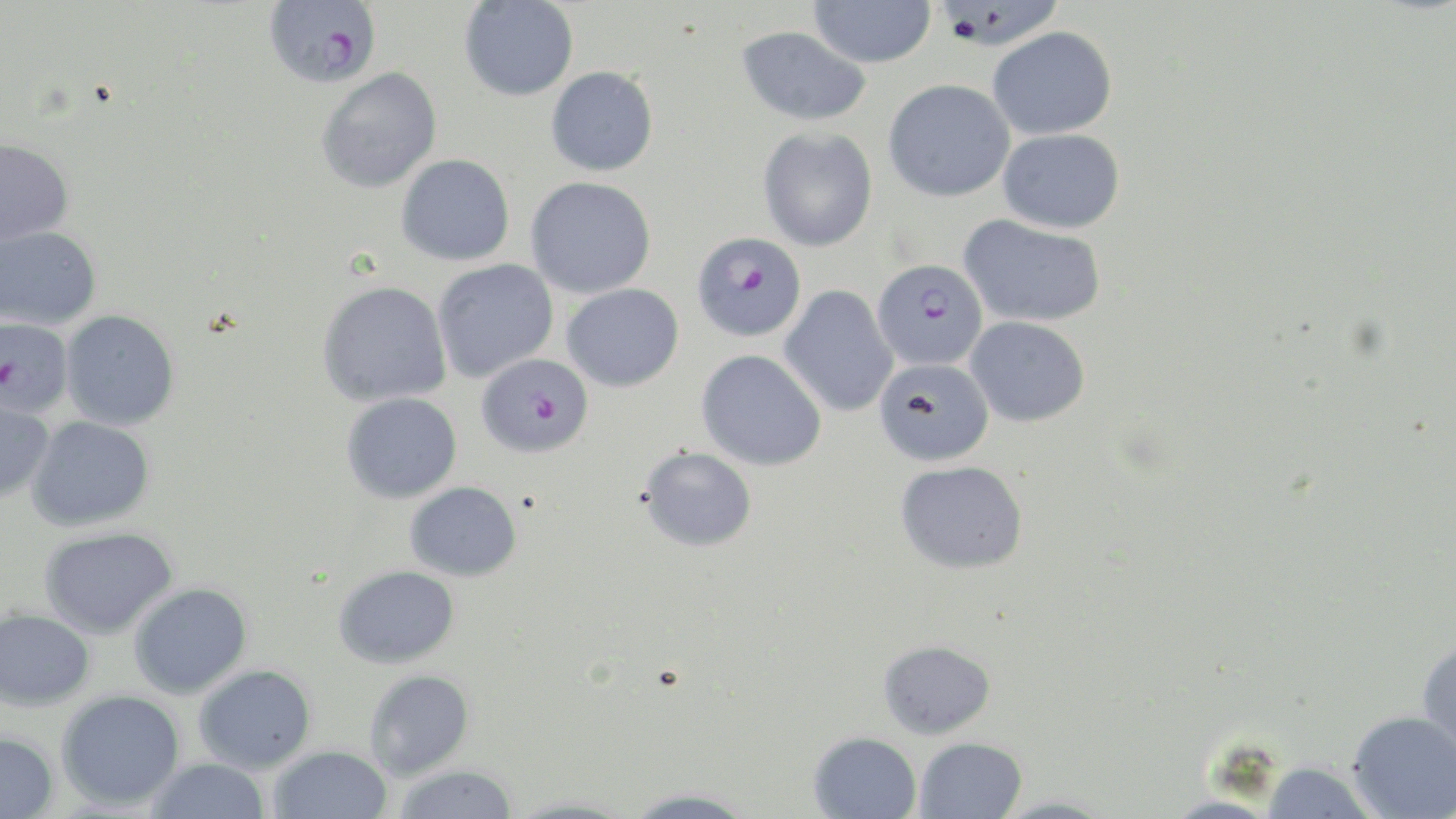 Approximate bounding boxes as (x1,y1)-(x2,y2) corner pairs in pixels. Uninfected red blood cell locations: (807,0)-(936,68), (459,1)-(578,101), (736,25)-(872,126), (986,26)-(1118,140), (546,66)-(658,176), (316,68)-(442,193), (883,79)-(1016,203), (757,127)-(878,251), (998,128)-(1127,233), (0,136)-(75,245), (397,154)-(515,265), (525,176)-(656,298), (959,213)-(1107,328), (0,225)-(102,329), (432,259)-(559,381), (317,280)-(452,407), (562,284)-(684,392), (779,285)-(898,417), (61,310)-(180,430), (966,316)-(1091,426), (696,350)-(826,471), (874,358)-(994,466), (341,392)-(462,504), (0,394)-(55,501), (26,416)-(155,531), (638,446)-(757,552), (894,460)-(1029,574), (405,481)-(522,581), (39,526)-(178,639), (333,565)-(460,668), (128,582)-(252,699), (0,608)-(96,710), (1416,637)-(1456,768), (878,639)-(995,738), (193,664)-(317,773), (363,669)-(475,780), (56,689)-(185,810), (1347,710)-(1456,819), (0,731)-(59,819), (807,731)-(922,819), (913,737)-(1027,819), (268,745)-(392,819), (145,756)-(271,818), (1260,761)-(1379,819), (391,763)-(520,819), (621,787)-(758,818), (992,794)-(1118,818). Plasmodium falciparum-infected red blood cell locations: (263,0)-(382,89), (692,232)-(806,342), (872,258)-(988,370), (0,315)-(74,419), (475,353)-(593,458). Slide-level diagnosis: Plasmodium falciparum. Light microscopy. May-Grünwald-Giemsa stain. Image is 1456×819 pixels. Thin blood film. One field of a larger specimen. Captured at 1000x magnification.